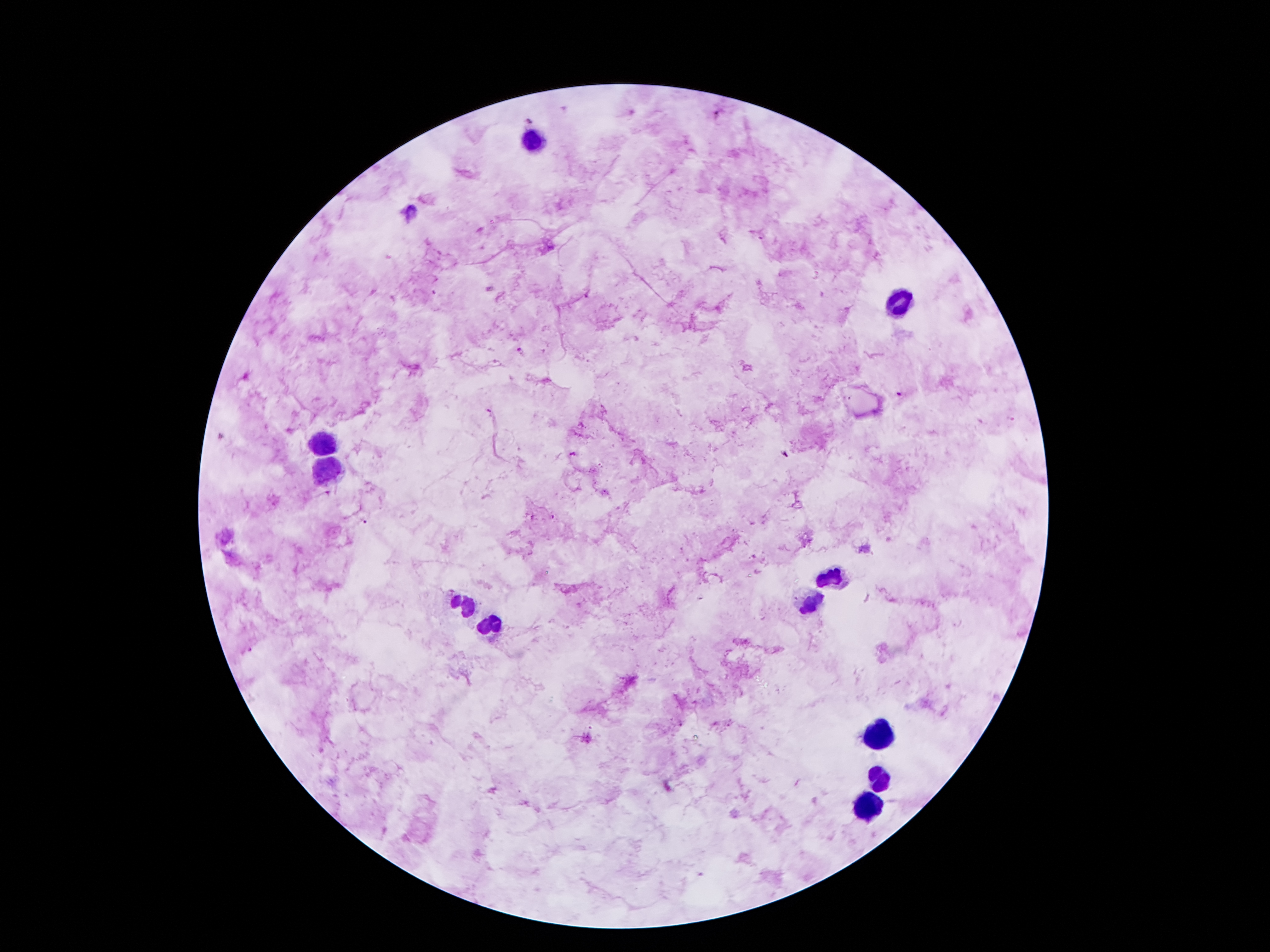

100x magnification. Photographed through the microscope eyepiece with a smartphone camera. Single field of view. Giemsa-stained preparation. Image is 1270×952 pixels. Thick peripheral-blood smear. Patient malaria status: positive for Plasmodium falciparum.